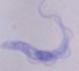
magnification = 1000x
modality = photomicrograph
identification = trypanosome